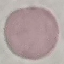
Summary:
  - Result: no malaria parasites seen
  - Capture: smartphone camera at the microscope eyepiece
  - Image type: automatically extracted cell patch, resized to 64 × 64 pixels
  - Preparation: thin smear
  - Stain: Giemsa